Give the position of each Plasmodium falciparum parasite with its life-cycle stage, each leukocyte, and any debris.
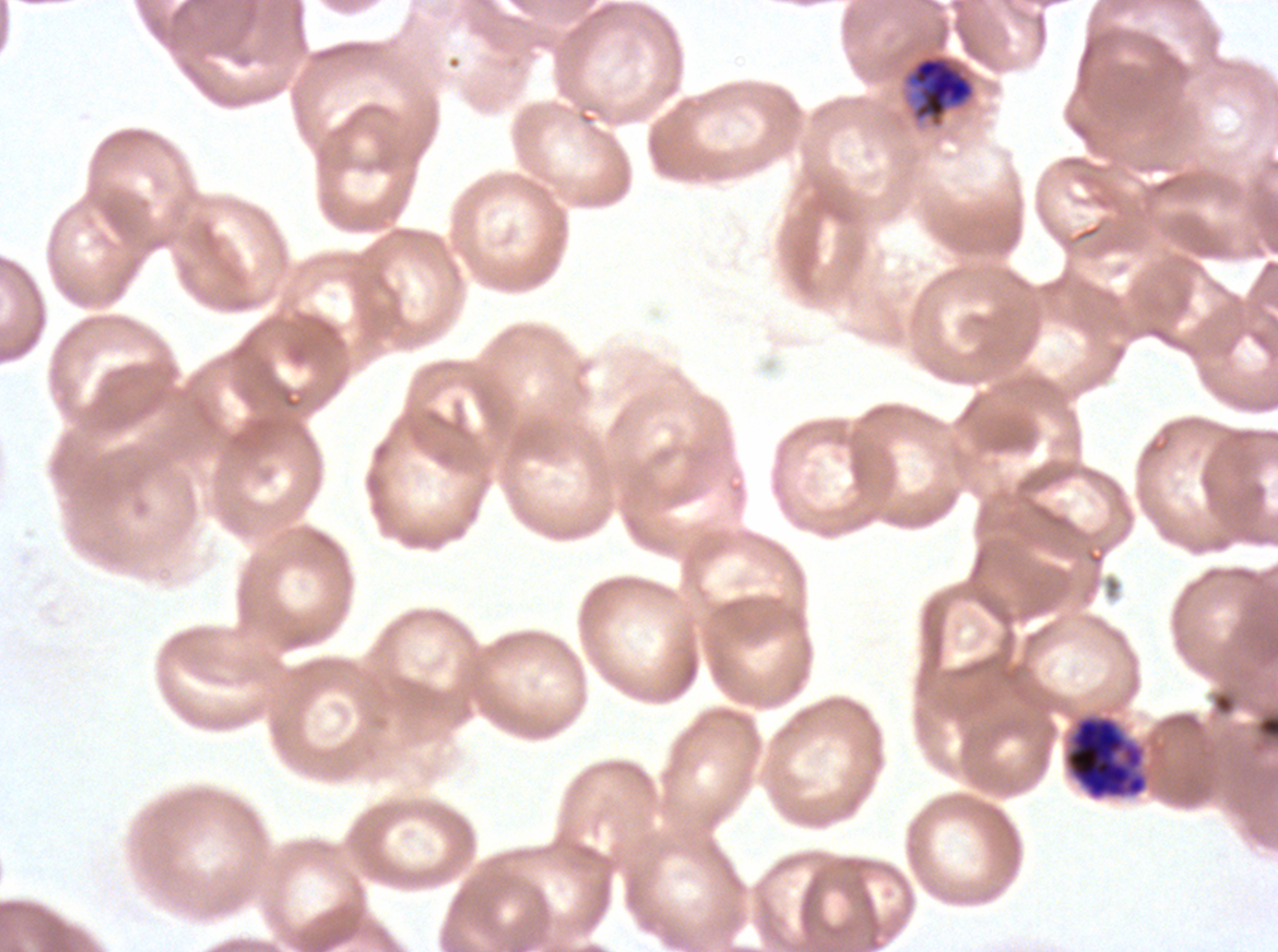
Approximate bounding boxes as {x1, y1, x2, y2} in pixels.
Late trophozoites: {907, 55, 975, 123}.
Late schizonts: {1065, 716, 1147, 799}.
No rings, late-ring/early-trophozoite forms, mid trophozoites, early schizonts, segmenters, gametocytes, leukocytes, or debris observed.

Giemsa-stained preparation. Plasmodium falciparum cultured ex vivo for 24 to 48 hours, from a patient in The Gambia. Life-cycle stages observed: late trophozoite, late schizont. Thin blood smear. Image is 1278×952 pixels. One sub-image of a larger composite.